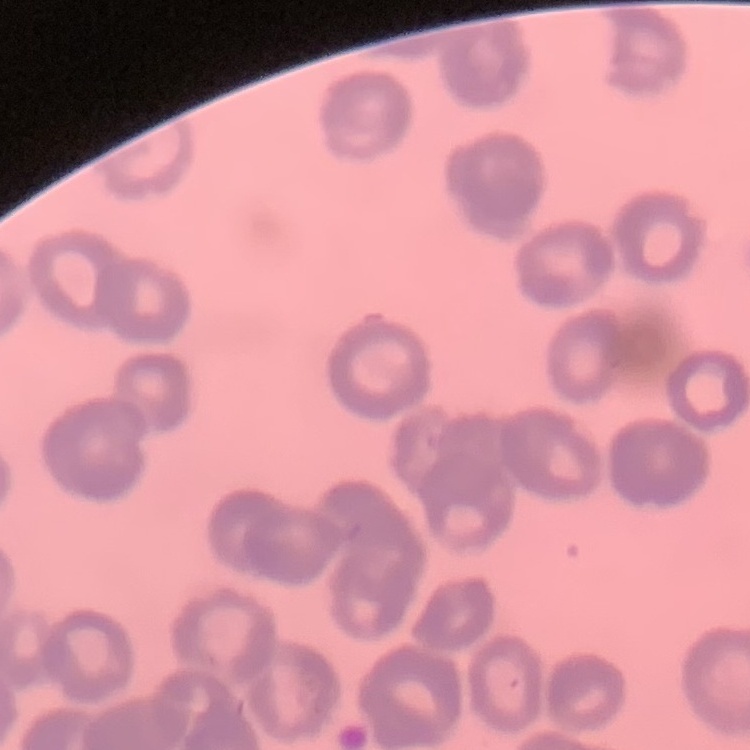
The red blood cells exhibit rouleaux formation. Square crop of a larger photomicrograph. Thin blood film. Stained with either Field's or Giemsa.